Locate every Plasmodium falciparum-infected red blood cell.
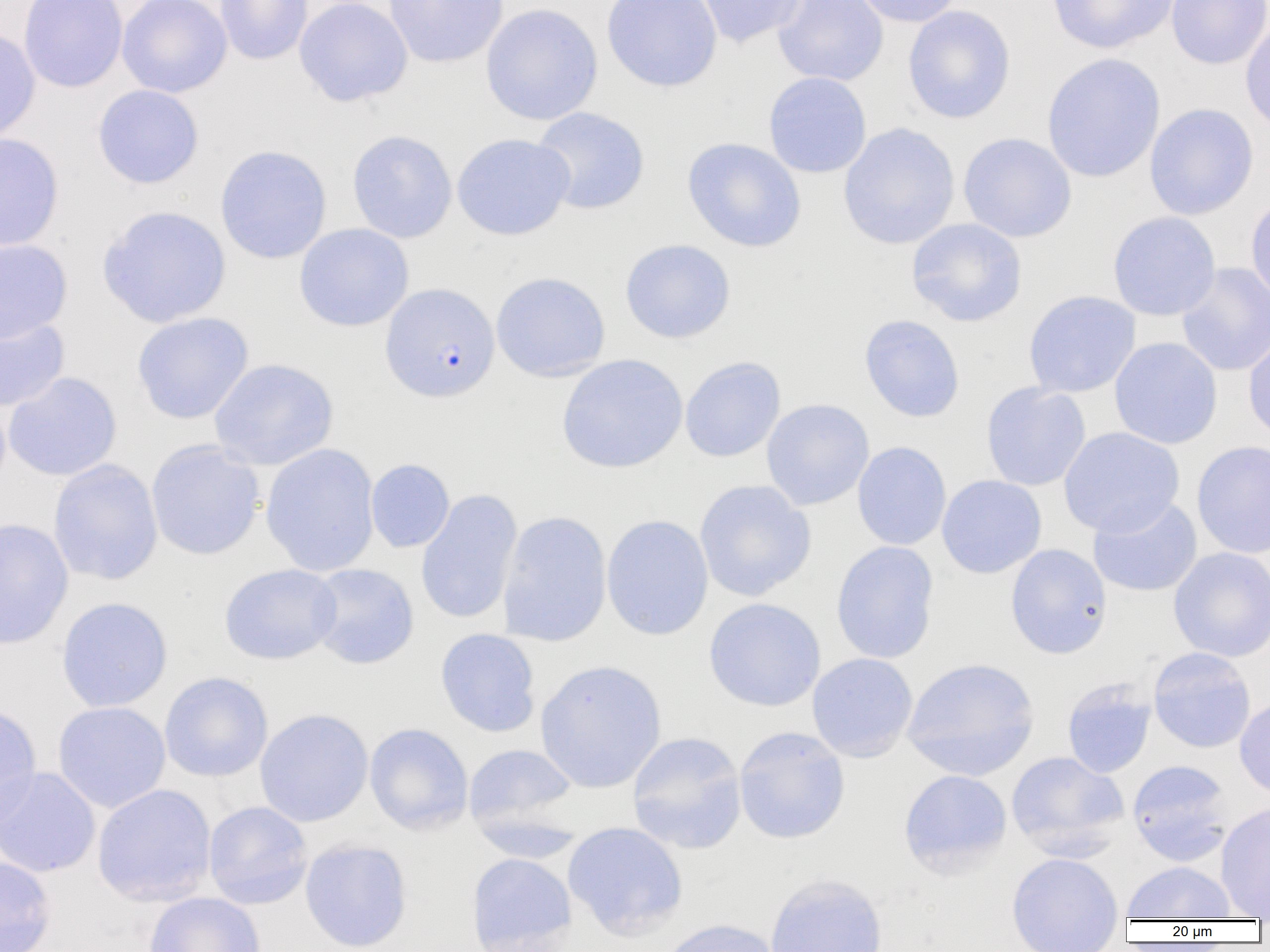

Approximate bounding boxes as named x1/y1/x2/y2 corners in pixels.
Plasmodium falciparum-infected red blood cells: (x1=379, y1=283, x2=500, y2=402).

slide_level_diagnosis: Plasmodium falciparum
uninfected_red_blood_cell_locations: 'approximate bounding boxes as named x1/y1/x2/y2 corners in pixels: (x1=19, y1=0, x2=128, y2=93), (x1=117, y1=0, x2=232, y2=97), (x1=215, y1=0, x2=314, y2=65), (x1=294, y1=0, x2=413, y2=107), (x1=383, y1=0, x2=509, y2=68), (x1=601, y1=0, x2=722, y2=92), (x1=695, y1=0, x2=808, y2=48), (x1=772, y1=0, x2=888, y2=86), (x1=850, y1=0, x2=965, y2=27), (x1=1046, y1=0, x2=1180, y2=55), (x1=1166, y1=0, x2=1270, y2=69), (x1=480, y1=3, x2=603, y2=126), (x1=902, y1=5, x2=1016, y2=124), (x1=1240, y1=17, x2=1270, y2=135), (x1=0, y1=27, x2=41, y2=144), (x1=1041, y1=53, x2=1165, y2=183), (x1=763, y1=72, x2=872, y2=178), (x1=92, y1=84, x2=204, y2=189), (x1=1144, y1=103, x2=1259, y2=220), (x1=530, y1=107, x2=650, y2=215), (x1=838, y1=122, x2=960, y2=250), (x1=347, y1=130, x2=457, y2=243), (x1=0, y1=132, x2=64, y2=251), (x1=958, y1=132, x2=1077, y2=243), (x1=451, y1=133, x2=574, y2=241), (x1=682, y1=137, x2=806, y2=252), (x1=214, y1=145, x2=333, y2=265), (x1=1245, y1=194, x2=1270, y2=304), (x1=97, y1=205, x2=231, y2=328), (x1=1107, y1=212, x2=1221, y2=321), (x1=906, y1=218, x2=1027, y2=327), (x1=293, y1=223, x2=414, y2=331), (x1=0, y1=239, x2=73, y2=343), (x1=620, y1=239, x2=736, y2=344), (x1=1176, y1=262, x2=1270, y2=377), (x1=490, y1=271, x2=611, y2=382), (x1=1023, y1=290, x2=1141, y2=398), (x1=0, y1=311, x2=70, y2=413), (x1=131, y1=312, x2=254, y2=424), (x1=859, y1=314, x2=965, y2=422), (x1=1243, y1=330, x2=1270, y2=444), (x1=1109, y1=337, x2=1223, y2=449), (x1=556, y1=353, x2=688, y2=474), (x1=679, y1=356, x2=786, y2=463), (x1=209, y1=358, x2=339, y2=471), (x1=2, y1=372, x2=122, y2=481), (x1=980, y1=382, x2=1091, y2=491), (x1=761, y1=398, x2=875, y2=511), (x1=1058, y1=426, x2=1185, y2=537), (x1=145, y1=439, x2=266, y2=561), (x1=1191, y1=440, x2=1270, y2=559), (x1=851, y1=441, x2=952, y2=550), (x1=259, y1=443, x2=380, y2=577), (x1=365, y1=458, x2=455, y2=553), (x1=48, y1=459, x2=163, y2=585), (x1=936, y1=475, x2=1047, y2=579), (x1=694, y1=479, x2=816, y2=602), (x1=416, y1=488, x2=523, y2=625), (x1=1088, y1=496, x2=1202, y2=597), (x1=498, y1=510, x2=612, y2=647), (x1=601, y1=514, x2=714, y2=641), (x1=0, y1=517, x2=74, y2=650), (x1=831, y1=541, x2=939, y2=664), (x1=1005, y1=543, x2=1112, y2=659), (x1=1168, y1=546, x2=1270, y2=662), (x1=219, y1=563, x2=342, y2=665), (x1=307, y1=563, x2=420, y2=669), (x1=55, y1=596, x2=173, y2=712), (x1=703, y1=597, x2=826, y2=712), (x1=435, y1=628, x2=541, y2=737), (x1=1147, y1=647, x2=1256, y2=753), (x1=806, y1=652, x2=918, y2=762), (x1=902, y1=656, x2=1040, y2=781), (x1=534, y1=659, x2=667, y2=793), (x1=159, y1=671, x2=273, y2=782), (x1=1062, y1=679, x2=1156, y2=778), (x1=1234, y1=695, x2=1270, y2=800), (x1=0, y1=701, x2=43, y2=831), (x1=52, y1=701, x2=171, y2=813), (x1=254, y1=708, x2=374, y2=827), (x1=364, y1=723, x2=474, y2=835), (x1=733, y1=726, x2=851, y2=844), (x1=627, y1=731, x2=748, y2=854), (x1=464, y1=743, x2=579, y2=840), (x1=1005, y1=750, x2=1130, y2=858), (x1=1127, y1=760, x2=1234, y2=866), (x1=0, y1=766, x2=100, y2=878), (x1=898, y1=769, x2=1013, y2=877), (x1=92, y1=783, x2=216, y2=906), (x1=203, y1=801, x2=313, y2=909), (x1=1215, y1=802, x2=1270, y2=918), (x1=562, y1=821, x2=688, y2=941), (x1=299, y1=838, x2=413, y2=952), (x1=1006, y1=851, x2=1124, y2=952), (x1=465, y1=852, x2=578, y2=952), (x1=0, y1=855, x2=56, y2=952), (x1=1121, y1=861, x2=1237, y2=921), (x1=764, y1=873, x2=888, y2=952), (x1=143, y1=891, x2=266, y2=952), (x1=658, y1=918, x2=785, y2=952)'
preparation: thin blood smear
image_size: 1270×952 pixels
modality: optical microscopy
field_of_view: single
magnification: 1000x